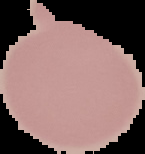

From a thin blood smear. Segmented cell region on a black background. Image is 145×154 pixels. Malaria status: uninfected.